Report the malaria status of this cell.
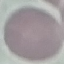

Uninfected.

Summary:
  - Image type: cell patch, automatically extracted from a larger field of view and resized to 64 × 64 pixels
  - Preparation: thin blood film
  - Stain: Giemsa
  - Capture: smartphone through the microscope eyepiece